Report the malaria status of this cell.
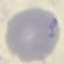

It is uninfected.

{
  "capture": "smartphone camera at the microscope eyepiece",
  "preparation": "thin blood smear",
  "stain": "Giemsa",
  "image_type": "cell patch, automatically extracted from a larger field of view and resized to 64 × 64 pixels"
}